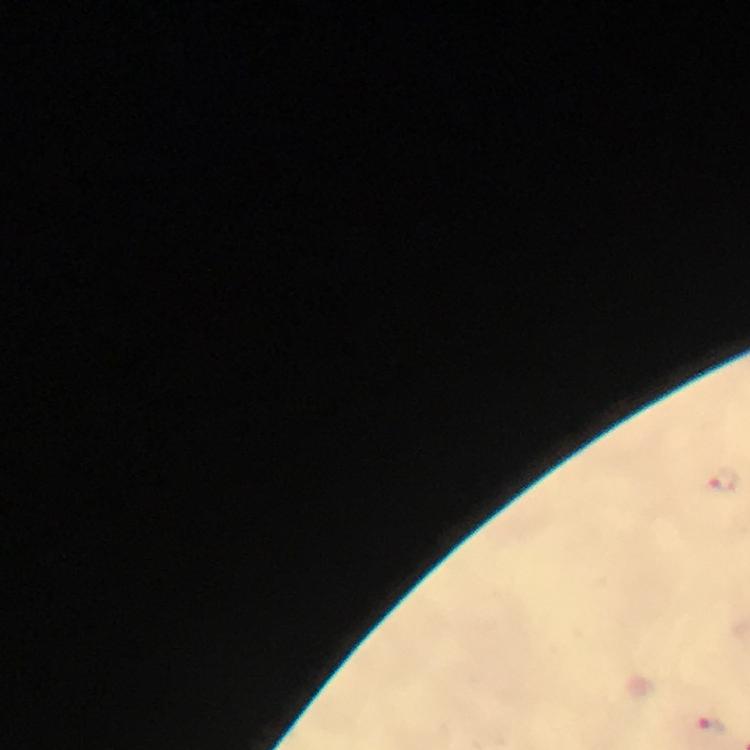

Approximate object centers, in pixels from the top-left corner.
Summary:
  - Plasmodium parasite locations: (x=724, y=479), (x=709, y=729)
  - Cropped from: one field of view
  - Capture: smartphone camera through the microscope
  - Image size: 750×750 pixels
  - Stain: Giemsa
  - Context: from a malaria diagnostic workup
  - Magnification: 100x
  - Immersion oil: used
  - Preparation: thick blood smear